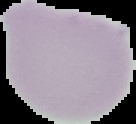 Cell region segmented out of the field of view; the surrounding area is masked to black. Image is 136×124 pixels. From a thin blood film. Result: no malaria parasites seen.